Classify this cell by malaria status.
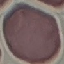

Uninfected.

Summary:
  - Capture: smartphone camera at the microscope eyepiece
  - Image type: automatically extracted cell patch, resized to 64 × 64 pixels
  - Preparation: thin smear
  - Stain: Giemsa